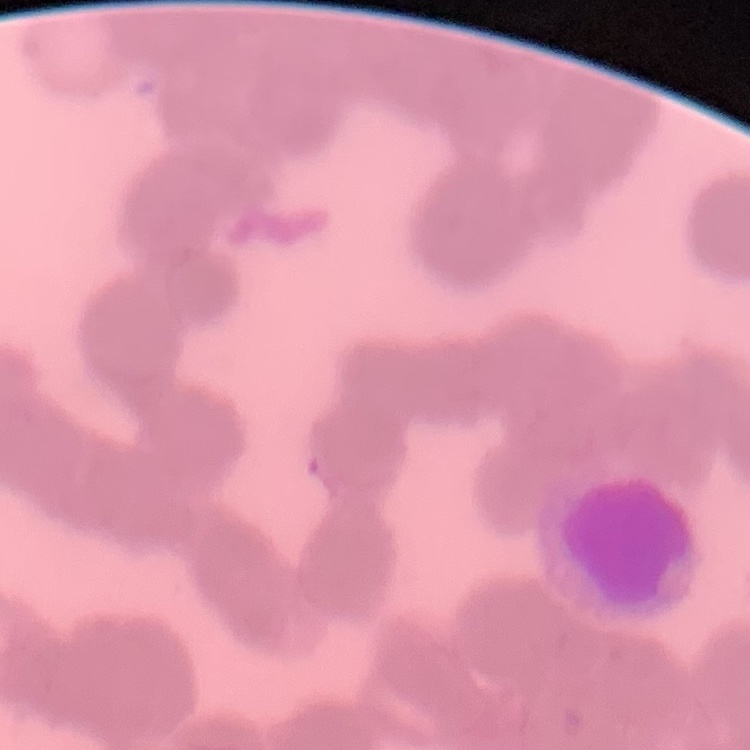
Summary:
  - Red blood cell morphology: rouleaux formation
  - Stain: Field's or Giemsa
  - Image type: one tile cut from a larger photomicrograph
  - Preparation: thin blood film